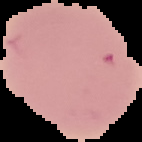

From a thin blood film. The area outside the segmented cell region is set to black. Result: negative for malaria parasites. Image is 142×142 pixels.